Describe the morphology of the red blood cells.
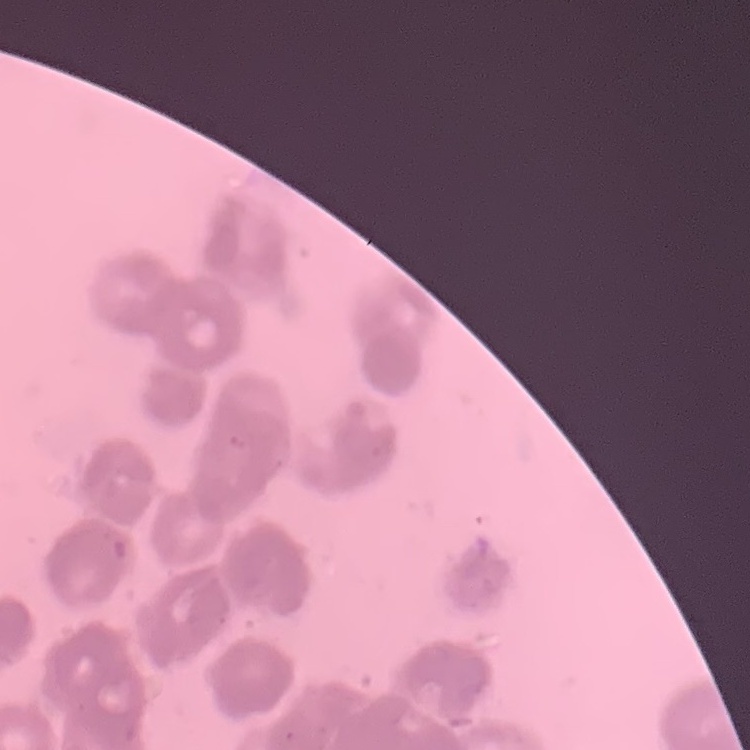

They show rouleaux formation.

Summary:
  - Preparation: thin blood smear
  - Image type: square crop of a larger photomicrograph
  - Stain: Field's or Giemsa